Assess this cell for malaria.
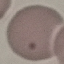

It is uninfected.

Thin smear of blood. Giemsa stain. Photographed with a smartphone camera at the microscope eyepiece. Automatically extracted cell patch, resized to 64 × 64 pixels.